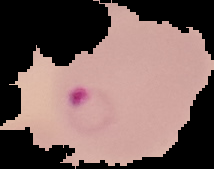
{
  "image_size": "214×169 pixels",
  "preparation": "thin blood film",
  "image_type": "segmented cell region with the area outside set to black",
  "result": "Plasmodium parasites identified"
}